Identify the blood parasite species.
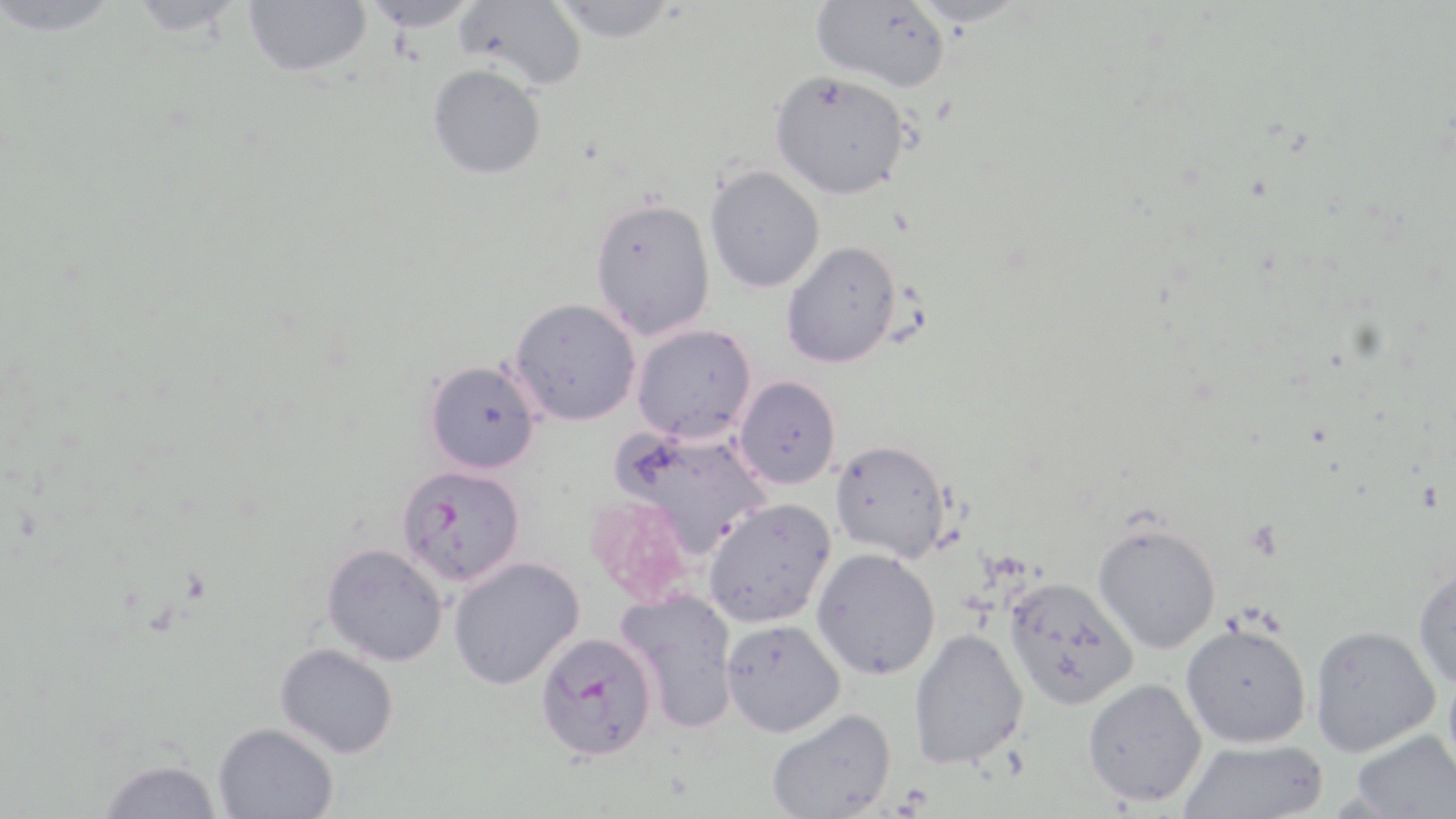
Plasmodium falciparum.

Approximate bounding boxes as (x1, y1, x2, y2) in pixels. Plasmodium falciparum-infected red blood cell locations: (397, 464, 526, 587), (536, 631, 657, 760). Uninfected red blood cell locations: (1, 0, 124, 36), (125, 0, 246, 37), (243, 0, 371, 77), (359, 0, 483, 32), (456, 0, 586, 92), (810, 0, 949, 93), (907, 0, 1029, 29), (548, 1, 680, 44), (427, 65, 546, 180), (770, 70, 911, 199), (705, 165, 825, 293), (589, 196, 717, 340), (781, 240, 902, 369), (510, 297, 642, 425), (632, 324, 757, 444), (423, 359, 542, 474), (734, 375, 841, 489), (612, 426, 773, 556), (829, 439, 952, 563), (703, 497, 836, 628), (1093, 520, 1221, 653), (321, 542, 448, 666), (812, 547, 941, 680), (447, 556, 584, 690), (1413, 560, 1456, 688), (1004, 575, 1139, 710), (614, 588, 740, 733), (721, 619, 845, 737), (1180, 622, 1311, 748), (1309, 626, 1441, 757), (908, 627, 1029, 769), (275, 643, 399, 758), (1082, 677, 1207, 806), (766, 708, 897, 819), (212, 722, 339, 819), (1350, 730, 1456, 818), (1178, 738, 1328, 818), (97, 758, 223, 819). Single field of view. Image is 1456×819 pixels. Light microscopy. May-Grünwald-Giemsa-stained preparation. 1000x magnification. Thin blood film.